Report the malaria status of this cell.
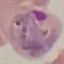

It is parasitized.

Summary:
  - Image type: cell patch, automatically extracted from a larger field of view and resized to 64 × 64 pixels
  - Preparation: thin smear
  - Stain: Giemsa
  - Capture: smartphone camera at the microscope eyepiece